Mark where leukocytes are.
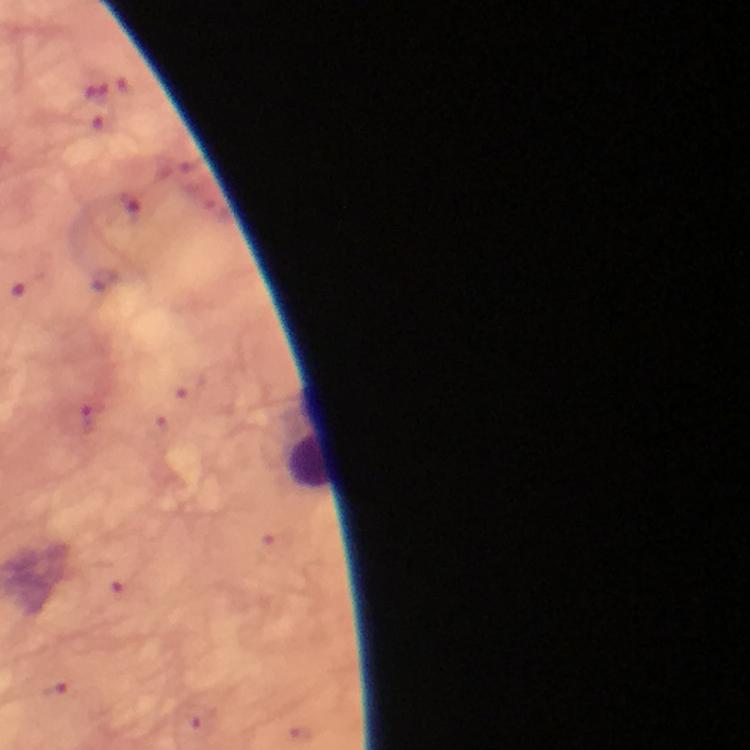
Approximate centers as {x, y} in pixels.
Leukocytes: {310, 457}.

capture: smartphone mounted on the microscope
preparation: thick smear
magnification: 100x
malaria_parasites: none seen
image_size: 750×750 pixels
stain: Giemsa
cropped_from: a single field of view
immersion_oil: used
context: from a malaria diagnostic workup